Report the malaria status of this cell.
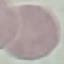

It is uninfected.

preparation: thin blood smear
stain: Giemsa
capture: smartphone through the microscope eyepiece
image_type: cell patch, automatically extracted from a larger field of view and resized to 64 × 64 pixels